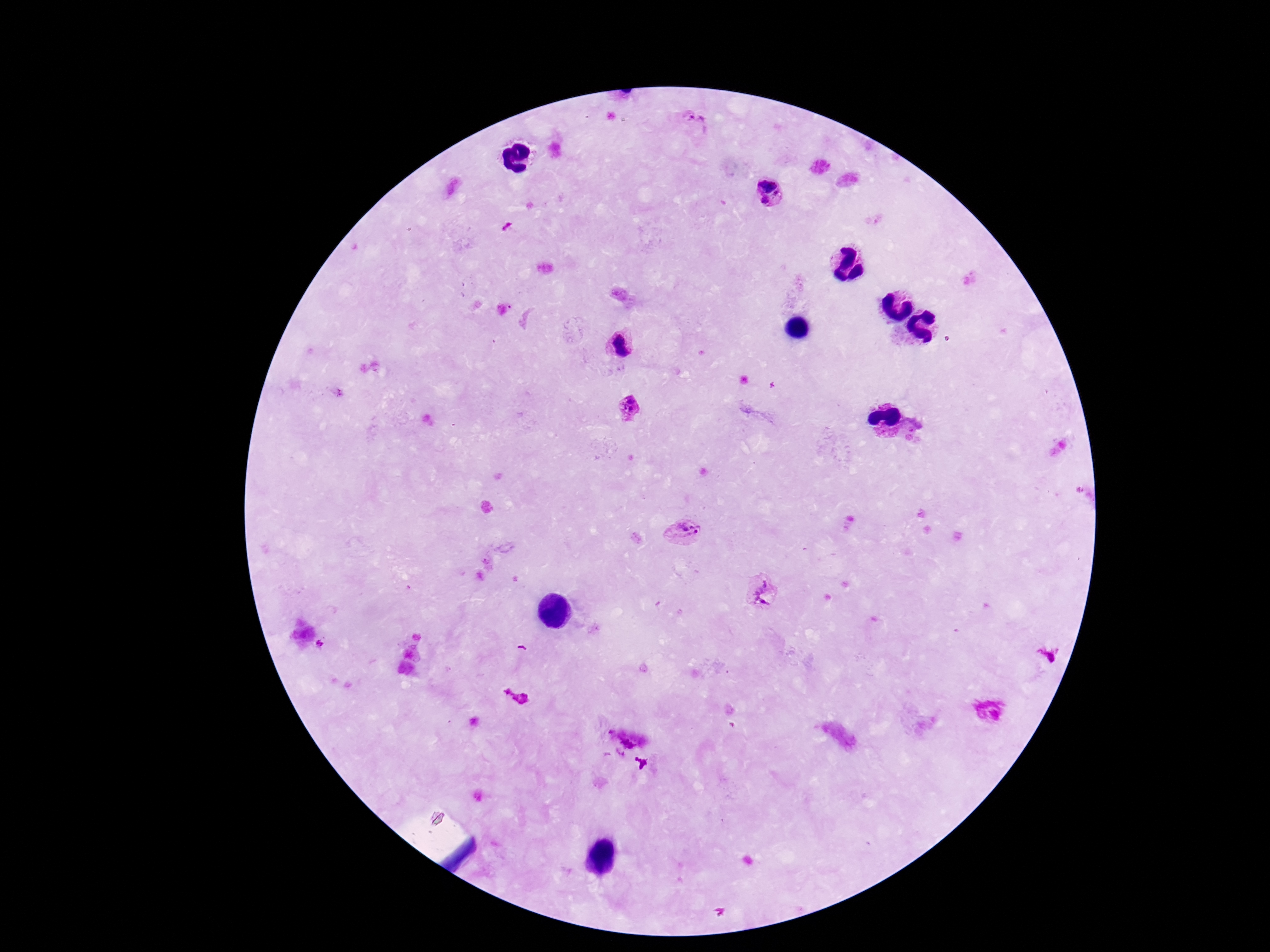
{
  "patient_malaria_status": "positive",
  "field_of_view": "single",
  "plasmodium_parasite_locations": "approximate centers as [x, y] in pixels: [696, 123], [769, 181], [765, 201], [622, 345], [628, 406], [687, 530], [763, 593], [1050, 656]",
  "image_size": "1270×952 pixels",
  "magnification": "100x",
  "preparation": "thick peripheral-blood smear",
  "capture": "smartphone camera through the microscope eyepiece",
  "stain": "Giemsa"
}